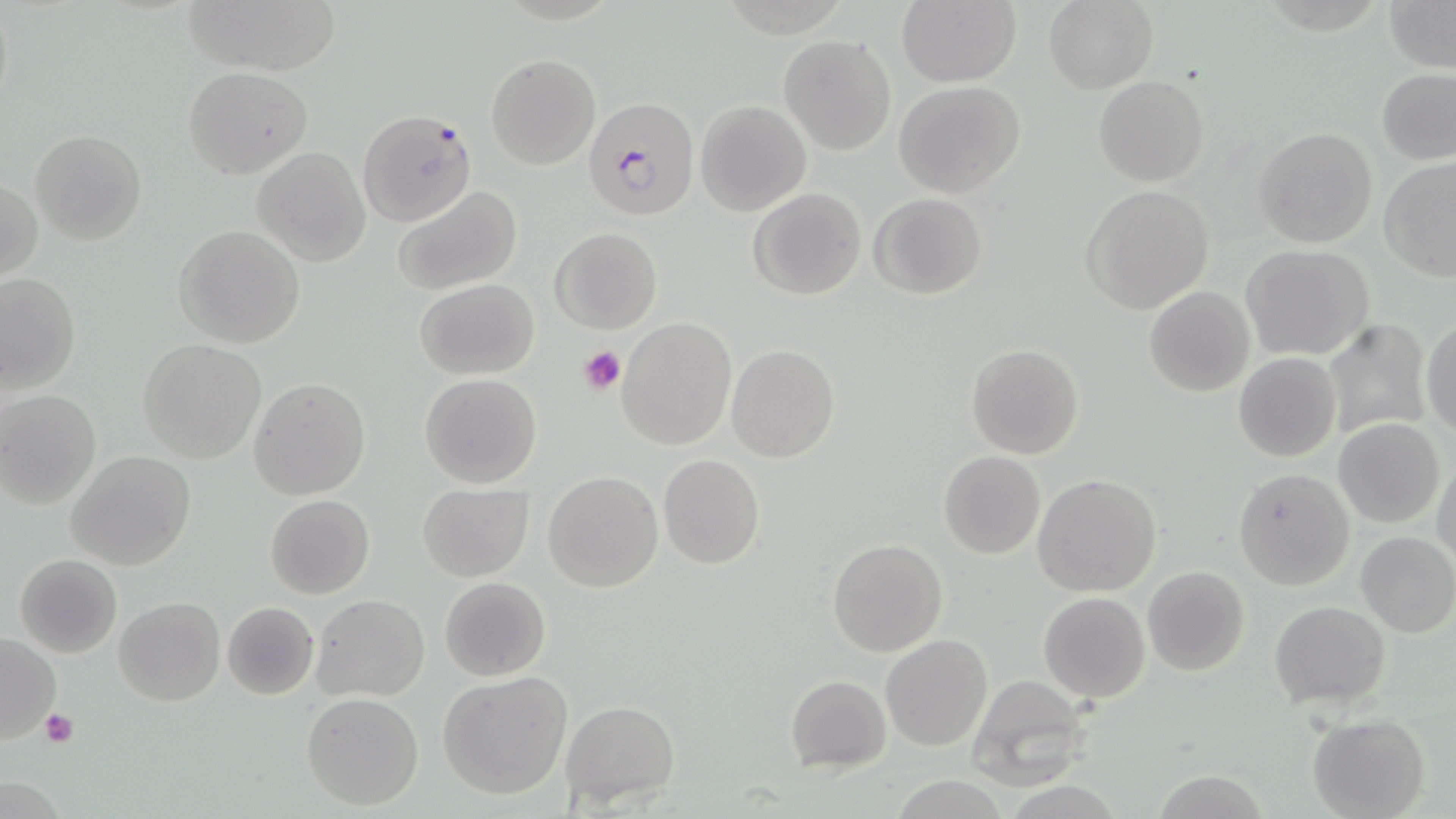 Approximate bounding boxes as (x1,y1)-(x2,y2) corner pairs in pixels. Plasmodium falciparum-infected red blood cell locations: (584,96)-(701,220), (359,108)-(475,225). Platelet locations: (580,345)-(627,394), (40,709)-(77,748). Uninfected red blood cell locations: (180,0)-(345,73), (897,0)-(1020,86), (1044,0)-(1159,94), (1383,0)-(1454,72), (778,34)-(896,155), (484,54)-(600,170), (184,66)-(313,179), (1377,69)-(1456,166), (1093,76)-(1209,185), (895,81)-(1025,199), (696,100)-(812,217), (1253,126)-(1378,250), (30,130)-(146,244), (253,146)-(370,266), (1378,157)-(1456,281), (2,177)-(41,284), (392,185)-(522,296), (1081,185)-(1214,316), (750,188)-(866,300), (870,193)-(987,300), (174,225)-(305,349), (551,227)-(661,334), (1241,245)-(1372,361), (0,274)-(81,397), (415,279)-(539,380), (1143,285)-(1255,397), (617,318)-(737,450), (1321,318)-(1432,442), (1421,318)-(1455,439), (138,339)-(266,463), (966,344)-(1084,459), (725,346)-(840,462), (1233,352)-(1341,462), (420,374)-(542,489), (249,379)-(371,500), (0,390)-(101,509), (1335,418)-(1446,527), (67,452)-(195,571), (939,452)-(1045,559), (658,455)-(766,570), (1432,456)-(1456,568), (1232,467)-(1355,591), (543,471)-(663,593), (1033,473)-(1161,596), (418,482)-(534,583), (265,494)-(374,598), (1356,531)-(1456,638), (827,537)-(947,656), (14,554)-(122,657), (1142,565)-(1251,678), (439,577)-(550,681), (1039,592)-(1150,703), (313,595)-(429,702), (116,597)-(225,706), (221,601)-(319,701), (1270,601)-(1390,708), (881,633)-(992,751), (0,634)-(60,743), (436,672)-(572,798), (786,674)-(892,772), (963,674)-(1098,788), (301,692)-(424,811), (560,700)-(680,808), (1308,714)-(1430,819). Slide-level diagnosis: Plasmodium falciparum. Thin blood smear. Image is 1456×819 pixels. Captured at 1000x magnification. Light microscopy. May-Grünwald-Giemsa stain. Single field of view.